Look for Plasmodium parasites.
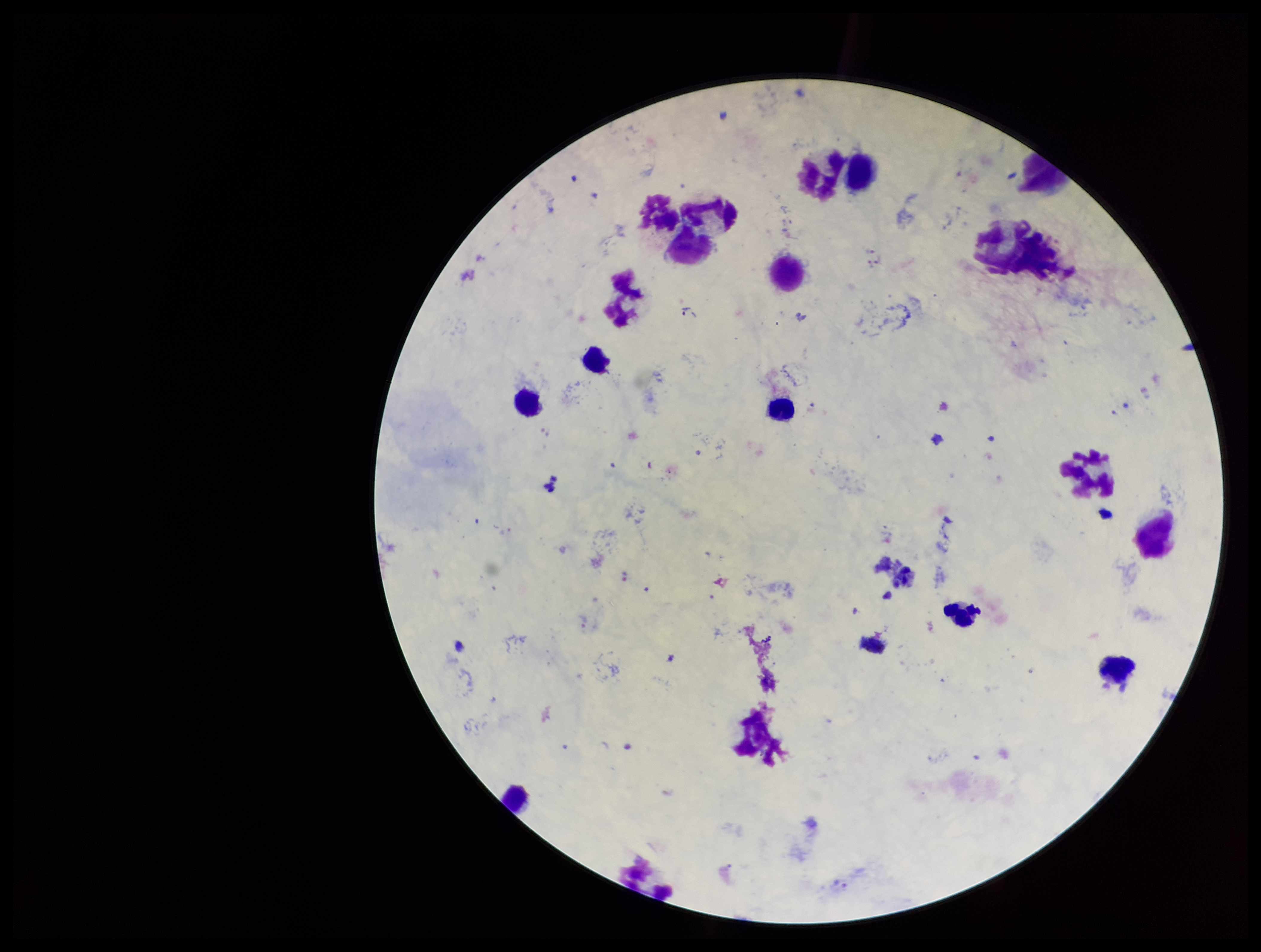
Seen.

Species reported for this patient: Plasmodium vivax. Preparation: thick smear. Smartphone photograph taken through the eyepiece of a microscope. Leukocyte count: 15. Image is 1261×952 pixels. Patient malaria status: infected. Stained with Giemsa. Single field of view. Parasite count: 1.